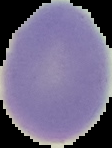
Summary:
  - Preparation: thin blood film
  - Image type: segmented cell region on a black background
  - Image size: 112×148 pixels
  - Result: no Plasmodium parasites detected